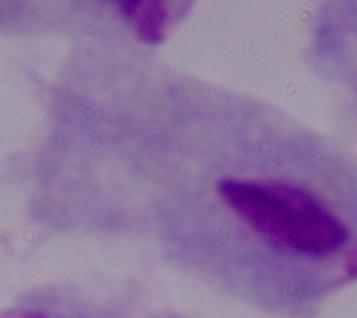
A trichomonad is seen. Photomicrograph. Captured at 1000x magnification.